Classify this cell by malaria status.
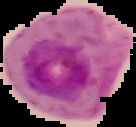
Parasitized.

image size = 136×127 pixels
image type = segmented cell region on a black background
preparation = thin blood film